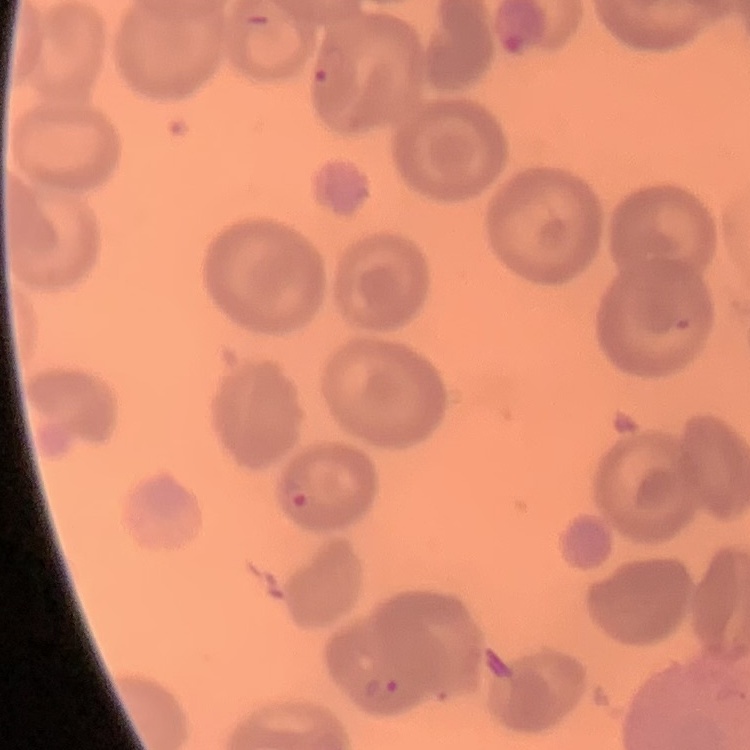
Summary:
  - Red blood cell morphology: no rouleaux formation
  - Image type: square crop of a larger photomicrograph
  - Stain: Field's or Giemsa
  - Preparation: thin blood smear